Assess this cell for malaria.
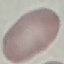

Uninfected.

Summary:
  - Capture: smartphone through the microscope eyepiece
  - Stain: Giemsa
  - Image type: automatically extracted cell patch, resized to 64 × 64 pixels
  - Preparation: thin smear